Locate the P. falciparum-infected red blood cells and any of indeterminate infection status.
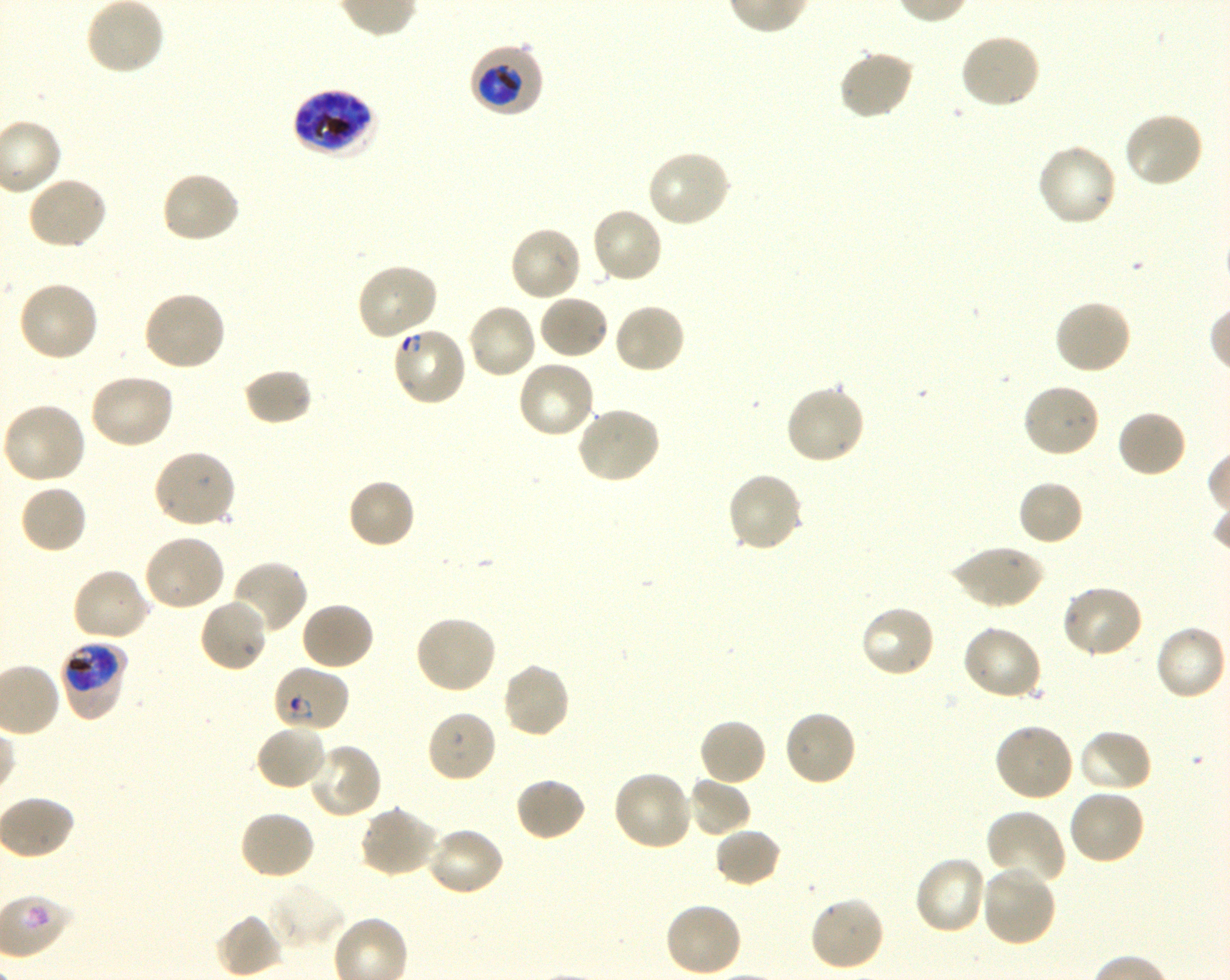
Approximate bounding rectangles given as corner coordinates in pixels from the top-left. Not every red blood cell is marked. A life-cycle stage — or a range of stages, where the recorded stages span more than one — follows each staged infected red blood cell.
Infected red blood cells: (x1=468, y1=42, x2=543, y2=118) trophozoite; (x1=292, y1=87, x2=379, y2=158) late trophozoite to late schizont; (x1=390, y1=325, x2=468, y2=408) ring; (x1=59, y1=640, x2=128, y2=722) trophozoite; (x1=270, y1=664, x2=351, y2=733) ring.
No red blood cells of indeterminate infection status observed.

locations of uninfected red blood cells = (x1=85, y1=0, x2=165, y2=76), (x1=958, y1=33, x2=1042, y2=111), (x1=838, y1=47, x2=916, y2=121), (x1=1122, y1=111, x2=1204, y2=190), (x1=1035, y1=142, x2=1119, y2=228), (x1=644, y1=150, x2=732, y2=230), (x1=160, y1=170, x2=241, y2=245), (x1=25, y1=175, x2=108, y2=251), (x1=589, y1=207, x2=664, y2=285), (x1=508, y1=224, x2=583, y2=303), (x1=354, y1=262, x2=438, y2=340), (x1=17, y1=280, x2=101, y2=363), (x1=143, y1=289, x2=227, y2=373), (x1=537, y1=293, x2=611, y2=360), (x1=1053, y1=298, x2=1133, y2=376), (x1=467, y1=302, x2=539, y2=380), (x1=612, y1=303, x2=687, y2=376), (x1=516, y1=358, x2=596, y2=439), (x1=243, y1=368, x2=314, y2=427), (x1=86, y1=372, x2=175, y2=451), (x1=1021, y1=382, x2=1101, y2=459), (x1=783, y1=384, x2=866, y2=466), (x1=0, y1=402, x2=87, y2=486), (x1=575, y1=406, x2=662, y2=484), (x1=1116, y1=409, x2=1188, y2=479), (x1=152, y1=448, x2=237, y2=530), (x1=725, y1=472, x2=805, y2=554), (x1=346, y1=478, x2=416, y2=550), (x1=1017, y1=480, x2=1084, y2=547), (x1=18, y1=483, x2=88, y2=554), (x1=142, y1=534, x2=227, y2=612), (x1=949, y1=544, x2=1045, y2=610), (x1=230, y1=559, x2=309, y2=636), (x1=70, y1=566, x2=152, y2=643), (x1=1060, y1=584, x2=1143, y2=661), (x1=198, y1=597, x2=270, y2=674), (x1=300, y1=601, x2=376, y2=671), (x1=857, y1=603, x2=936, y2=680), (x1=412, y1=614, x2=497, y2=695), (x1=960, y1=623, x2=1045, y2=701), (x1=1154, y1=623, x2=1227, y2=701), (x1=500, y1=661, x2=571, y2=739), (x1=783, y1=708, x2=858, y2=788), (x1=426, y1=710, x2=498, y2=784), (x1=698, y1=717, x2=767, y2=787), (x1=992, y1=722, x2=1074, y2=803), (x1=254, y1=723, x2=329, y2=792), (x1=1076, y1=729, x2=1153, y2=794), (x1=307, y1=741, x2=383, y2=819), (x1=611, y1=769, x2=693, y2=852), (x1=514, y1=776, x2=588, y2=843), (x1=687, y1=777, x2=753, y2=837), (x1=1067, y1=788, x2=1146, y2=866), (x1=358, y1=805, x2=439, y2=879), (x1=985, y1=808, x2=1066, y2=887), (x1=238, y1=810, x2=316, y2=882), (x1=425, y1=825, x2=506, y2=897), (x1=713, y1=827, x2=782, y2=888), (x1=913, y1=856, x2=989, y2=937), (x1=980, y1=864, x2=1058, y2=947), (x1=266, y1=880, x2=345, y2=951), (x1=808, y1=896, x2=886, y2=973), (x1=663, y1=900, x2=743, y2=978), (x1=215, y1=913, x2=282, y2=978)
life-cycle stages observed = ring, trophozoite
preparation = thin blood smear
field of view = single
culture = P. falciparum strain 3D7, shaking, in vitro
donor blood group = O+
image size = 1230×980 pixels
stain = Giemsa
objective = 100x, oil immersion, numerical aperture 1.30